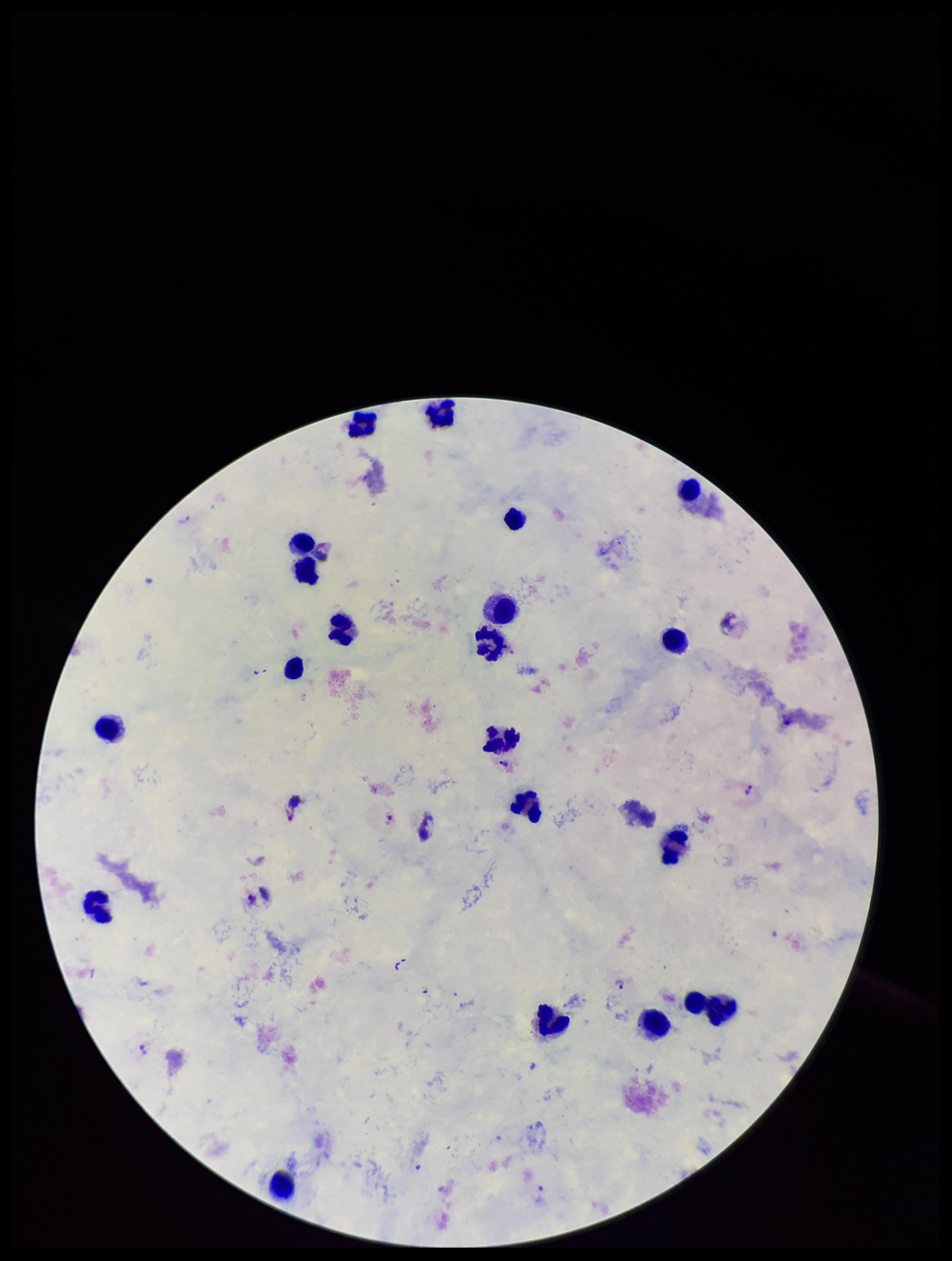

Summary:
  - Parasite count: 5
  - Capture: smartphone photograph through the microscope eyepiece
  - Leukocyte count: 21
  - Plasmodium parasites: seen
  - Patient malaria status: infected
  - Species reported for this patient: Plasmodium vivax
  - Field of view: single
  - Stain: Giemsa
  - Preparation: thick smear
  - Image size: 952×1261 pixels